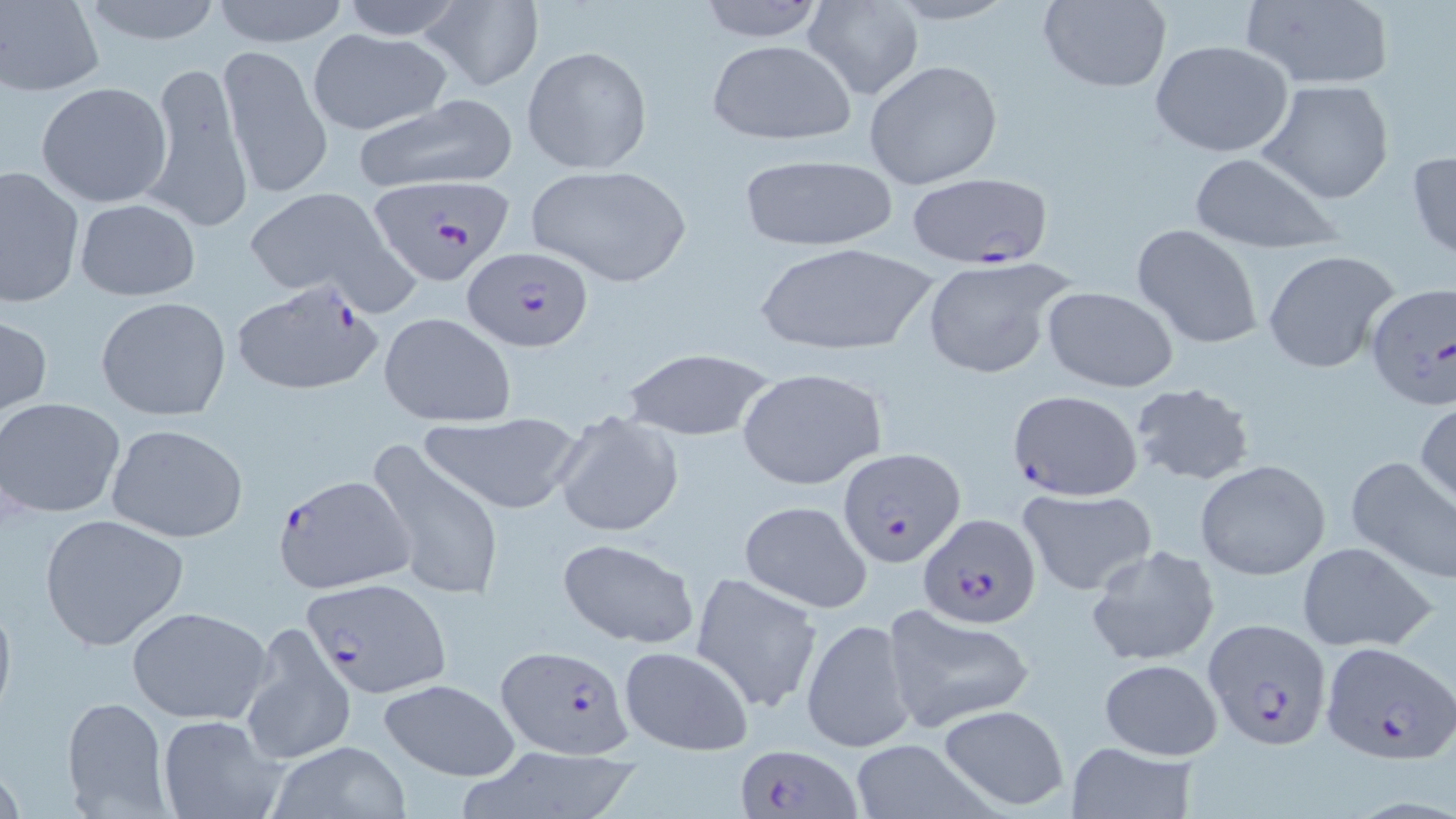
Summary:
  - Coordinate format: approximate bounding boxes as (x1,y1)-(x2,y2) corner pairs in pixels
  - Plasmodium falciparum-infected red blood cell locations: (906,171)-(1054,269), (368,173)-(516,285), (461,246)-(594,352), (230,278)-(385,396), (1364,284)-(1456,411), (1008,388)-(1143,499), (836,445)-(963,568), (271,472)-(412,594), (918,513)-(1039,629), (301,577)-(451,697), (1202,619)-(1332,749), (1320,640)-(1455,765), (494,646)-(632,758), (734,741)-(861,819)
  - Uninfected red blood cell locations: (1,0)-(105,94), (72,0)-(232,48), (208,0)-(354,48), (333,0)-(472,38), (692,0)-(829,42), (1035,0)-(1172,93), (1239,0)-(1395,90), (420,1)-(545,92), (804,1)-(923,101), (306,30)-(453,133), (705,38)-(857,146), (1150,39)-(1295,159), (218,43)-(332,200), (522,46)-(652,174), (864,60)-(1004,190), (144,63)-(252,235), (1258,79)-(1396,204), (35,82)-(175,208), (349,92)-(520,195), (1407,147)-(1456,263), (1185,154)-(1343,252), (736,155)-(899,254), (0,164)-(85,309), (524,164)-(693,288), (239,185)-(408,308), (72,198)-(200,302), (1131,223)-(1266,349), (753,242)-(939,358), (1263,249)-(1400,375), (921,257)-(1074,380), (1041,285)-(1179,392), (95,296)-(232,421), (0,312)-(51,419), (378,312)-(515,426), (621,348)-(775,442), (737,367)-(886,490), (1129,381)-(1257,487), (1,396)-(126,519), (1415,398)-(1456,508), (551,409)-(685,539), (420,412)-(583,515), (104,422)-(247,542), (365,437)-(504,604), (1344,454)-(1456,584), (1195,459)-(1331,580), (1015,486)-(1156,596), (739,498)-(874,613), (38,512)-(191,651), (555,536)-(700,649), (1296,541)-(1440,653), (1086,543)-(1221,668), (690,572)-(822,713), (0,586)-(17,729), (125,605)-(272,724), (883,605)-(1034,730), (801,617)-(917,754), (240,623)-(355,768), (617,645)-(753,754), (1097,658)-(1224,760), (375,677)-(523,783), (60,696)-(171,815), (937,704)-(1070,811), (157,714)-(287,819), (1064,741)-(1199,819), (849,742)-(992,816), (271,743)-(412,816), (462,747)-(645,819)
  - Slide-level diagnosis: Plasmodium falciparum
  - Preparation: thin blood smear
  - Magnification: 1000x
  - Image size: 1456×819 pixels
  - Field of view: one of a larger specimen
  - Stain: May-Grünwald-Giemsa
  - Modality: light microscopy